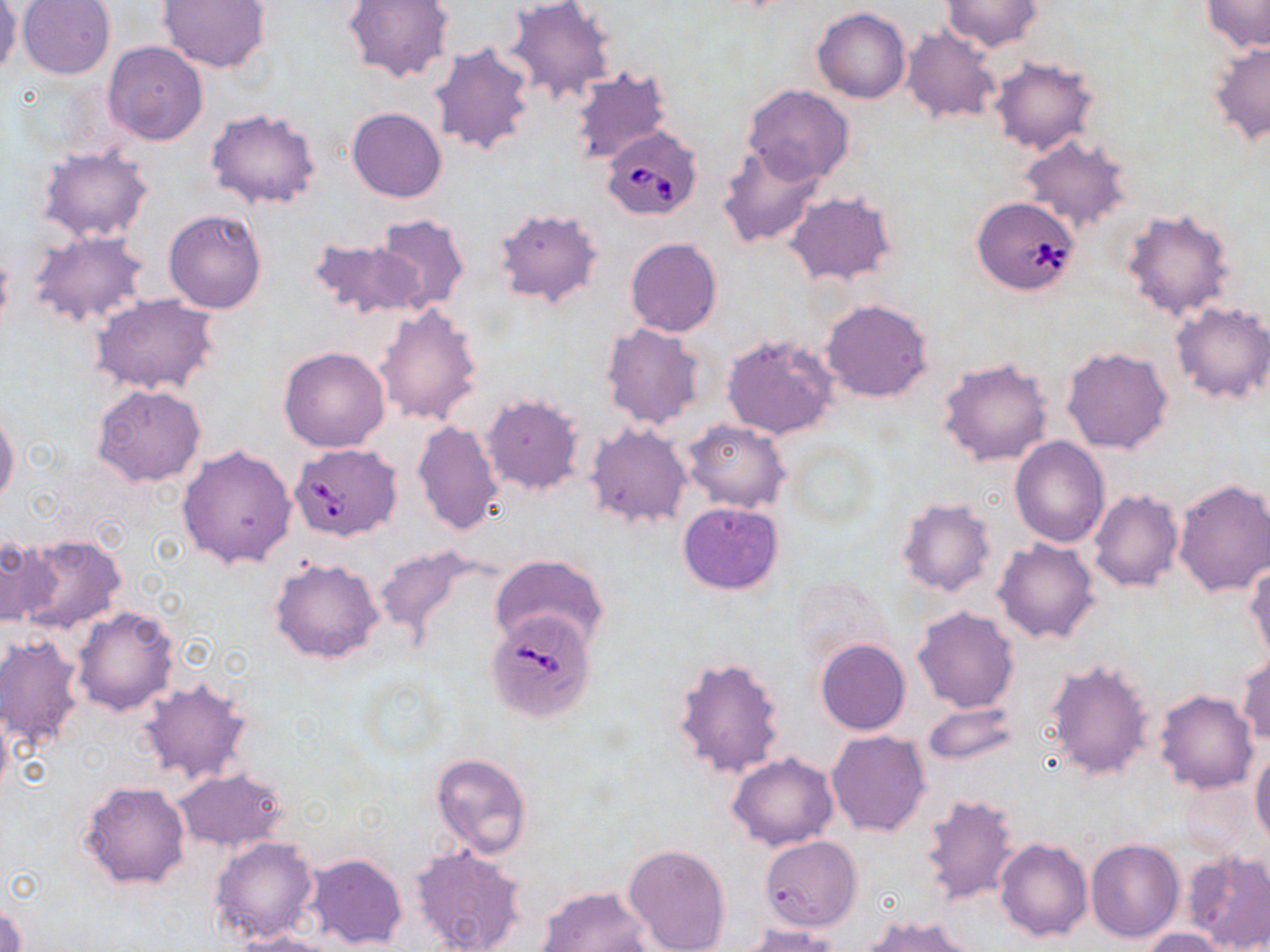
Approximate bounding boxes as (x1,y1)-(x2,y2) corner pairs in pixels. Uninfected red blood cell locations: (157,0)-(271,74), (343,0)-(453,83), (505,0)-(616,103), (1202,0)-(1270,52), (19,1)-(115,79), (941,1)-(1043,52), (1,3)-(23,79), (812,9)-(910,103), (901,25)-(1001,125), (103,40)-(208,146), (430,41)-(537,159), (1208,43)-(1270,144), (988,55)-(1100,156), (568,67)-(672,166), (743,84)-(855,184), (347,107)-(448,202), (205,108)-(321,211), (1017,133)-(1131,233), (716,142)-(826,249), (37,145)-(156,244), (786,191)-(899,287), (492,206)-(604,310), (1121,207)-(1238,321), (164,208)-(268,314), (371,212)-(470,312), (25,230)-(149,328), (310,234)-(423,320), (625,238)-(722,338), (0,249)-(13,336), (90,293)-(221,397), (821,299)-(932,403), (1169,301)-(1270,407), (373,302)-(484,427), (600,321)-(707,429), (722,333)-(839,440), (278,346)-(390,453), (1060,346)-(1174,456), (937,357)-(1054,466), (92,385)-(206,486), (482,394)-(585,497), (0,409)-(20,509), (413,419)-(503,535), (684,419)-(789,513), (586,423)-(692,527), (786,436)-(880,530), (1009,436)-(1109,546), (177,444)-(296,569), (1173,479)-(1270,596), (1088,489)-(1184,593), (897,497)-(997,596), (678,501)-(784,595), (17,533)-(126,635), (0,535)-(62,626), (994,538)-(1101,644), (372,544)-(490,647), (491,555)-(609,651), (269,556)-(384,665), (1245,559)-(1270,664), (792,579)-(894,669), (72,605)-(178,716), (913,607)-(1018,713), (0,632)-(87,758), (815,639)-(910,735), (1236,652)-(1269,746), (672,655)-(786,780), (1045,660)-(1154,782), (137,679)-(255,787), (1154,690)-(1258,793), (0,700)-(13,803), (922,701)-(1019,766), (825,730)-(931,836), (430,751)-(533,859), (1251,751)-(1270,846), (727,753)-(840,852), (173,768)-(289,853), (1174,777)-(1254,860), (79,780)-(191,890), (919,792)-(1022,906), (210,835)-(319,945), (761,836)-(862,932), (994,838)-(1093,944), (1085,838)-(1185,945), (410,842)-(529,952), (623,843)-(731,952), (1185,850)-(1270,952), (306,853)-(408,949), (535,885)-(652,951), (1,903)-(25,952), (860,915)-(977,952), (741,923)-(844,951), (1140,928)-(1230,951), (236,932)-(342,952). Babesia divergens-infected red blood cell locations: (600,125)-(705,220), (970,196)-(1080,296), (288,443)-(402,541), (487,612)-(596,724). Slide-level diagnosis: Babesia divergens. May-Grünwald-Giemsa stain. Captured at 1000x magnification. Image is 1270×952 pixels. Optical microscopy. One field of a larger specimen. Thin blood smear.